State which parasite is depicted.
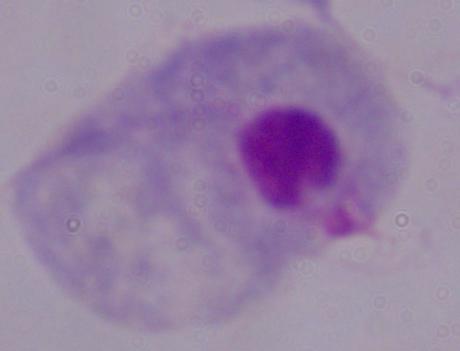
A trichomonad.

modality = micrograph
magnification = 1000x